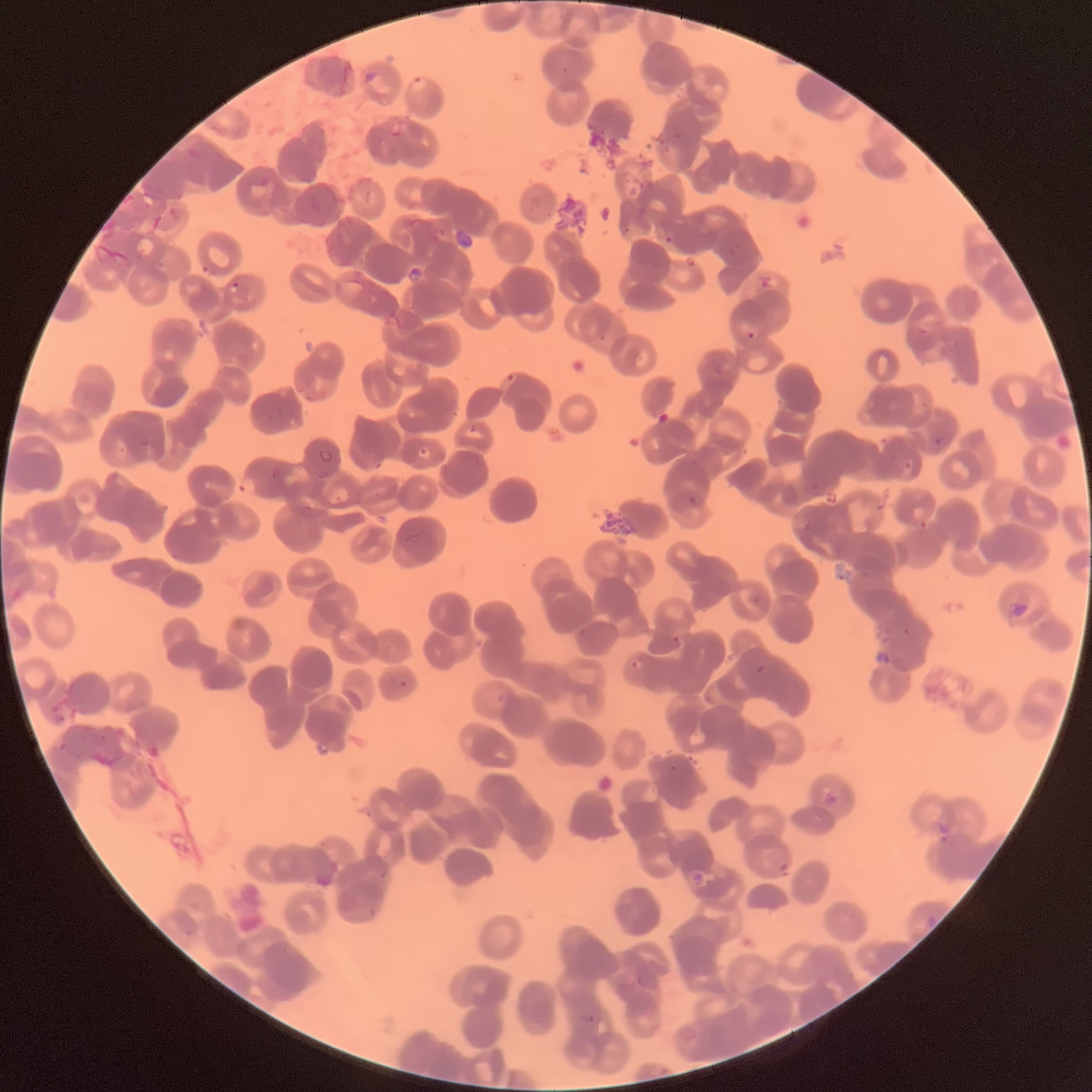
coordinate format = approximate bounding boxes as named x1/y1/x2/y2 corners in pixels
Plasmodium parasites too small for a box (approximate object centers, named x/y in pixels) = (x=945, y=839)
Plasmodium parasite locations = (x1=408, y1=77, x2=428, y2=93), (x1=663, y1=235, x2=674, y2=246), (x1=229, y1=282, x2=240, y2=295), (x1=745, y1=328, x2=759, y2=343), (x1=503, y1=372, x2=519, y2=387), (x1=935, y1=437, x2=942, y2=445), (x1=237, y1=473, x2=258, y2=497), (x1=400, y1=681, x2=408, y2=687), (x1=637, y1=974, x2=649, y2=987), (x1=582, y1=1013, x2=596, y2=1025)
red blood cell morphology = rouleaux formation
modality = optical microscopy
image size = 1092×1092 pixels
preparation = thin blood film